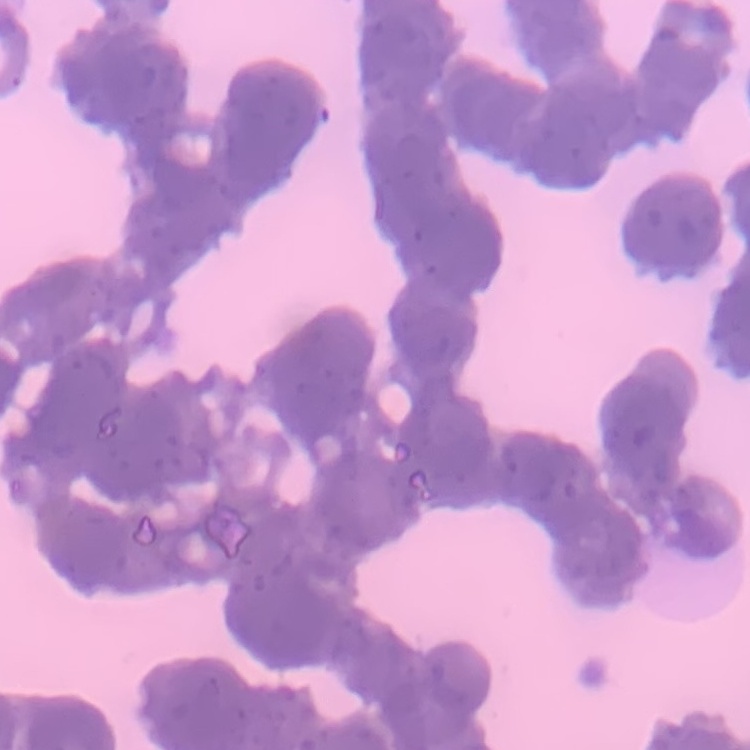 The red blood cells show rouleaux formation. Field's or Giemsa stain. Thin blood smear. One tile cut from a larger photomicrograph.